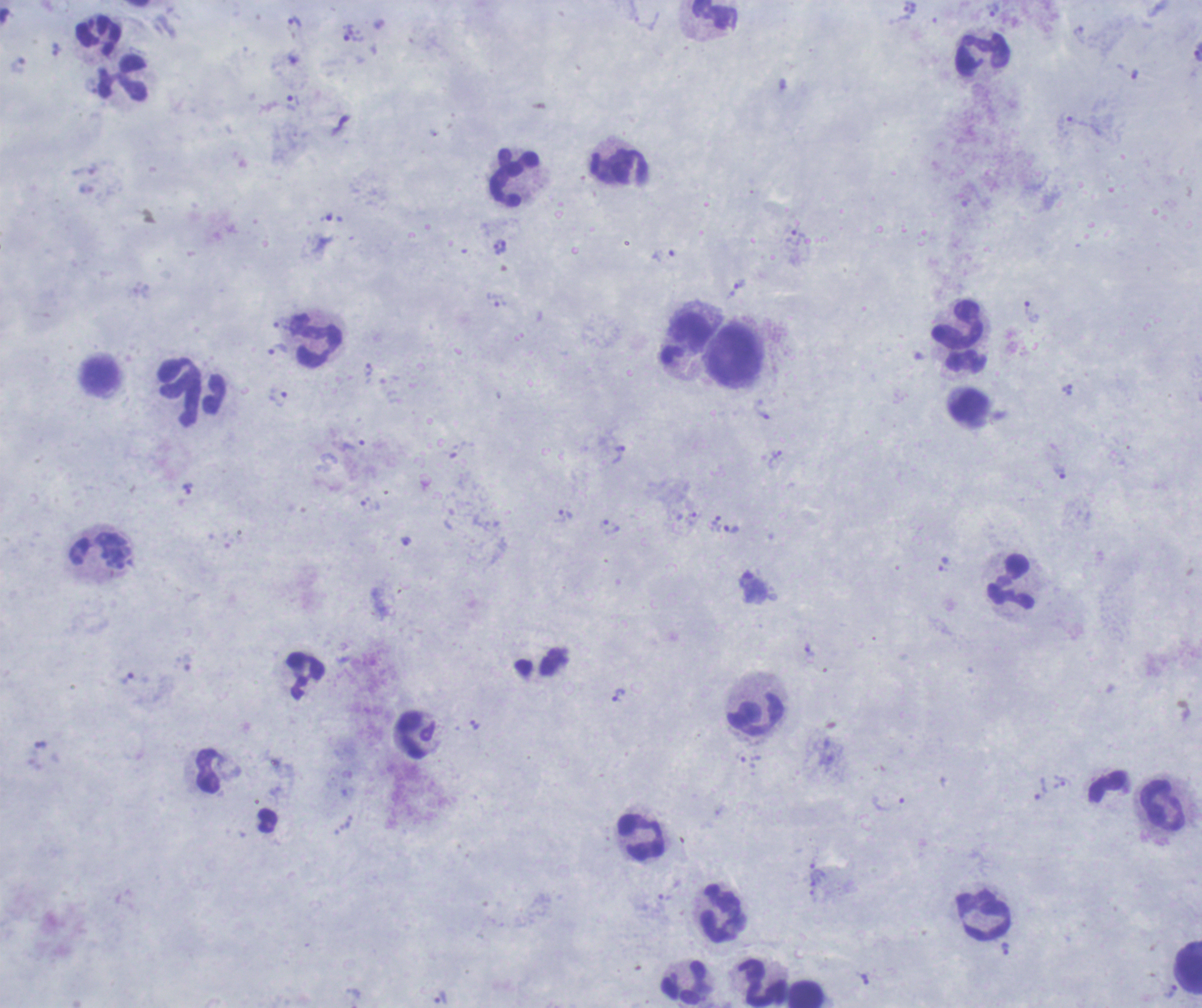 Thick blood smear. Romanowsky stain. One field from this slide. Image is 1202×1008 pixels.